Identify the cell.
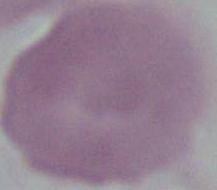

This is an erythrocyte.

1000x magnification. Photomicrograph.